Classify this cell by malaria status.
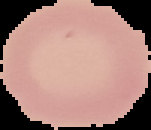
Uninfected.

Image is 151×130 pixels. The area outside the segmented cell region is set to black. From a thin blood smear.